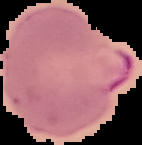

Summary:
  - Image size: 142×145 pixels
  - Image type: segmented cell region with the area outside set to black
  - Preparation: thin blood smear
  - Result: Plasmodium parasites identified